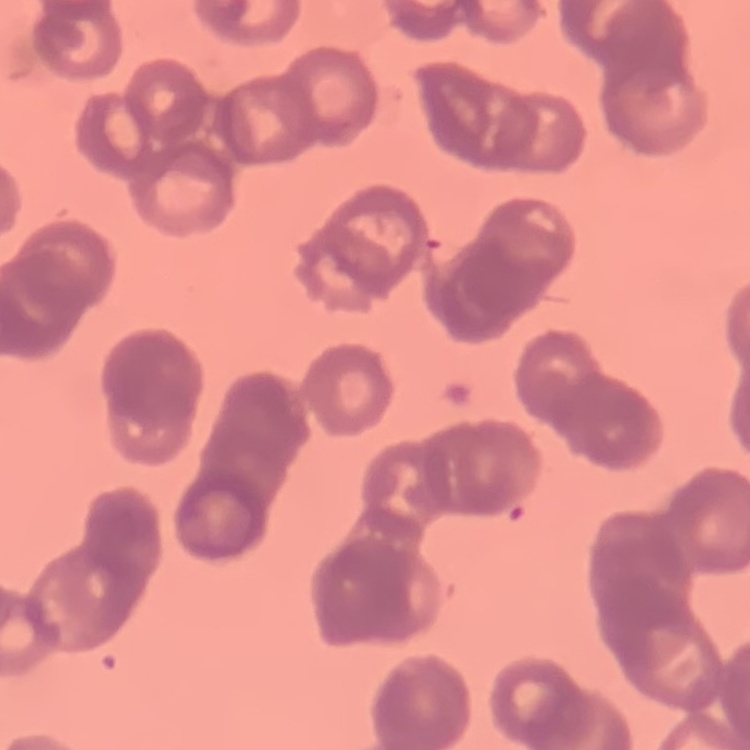 The erythrocytes exhibit rouleaux formation. Thin blood smear. Stained with either Field's or Giemsa. One tile cut from a larger photomicrograph.